Comment on the morphology of the erythrocytes.
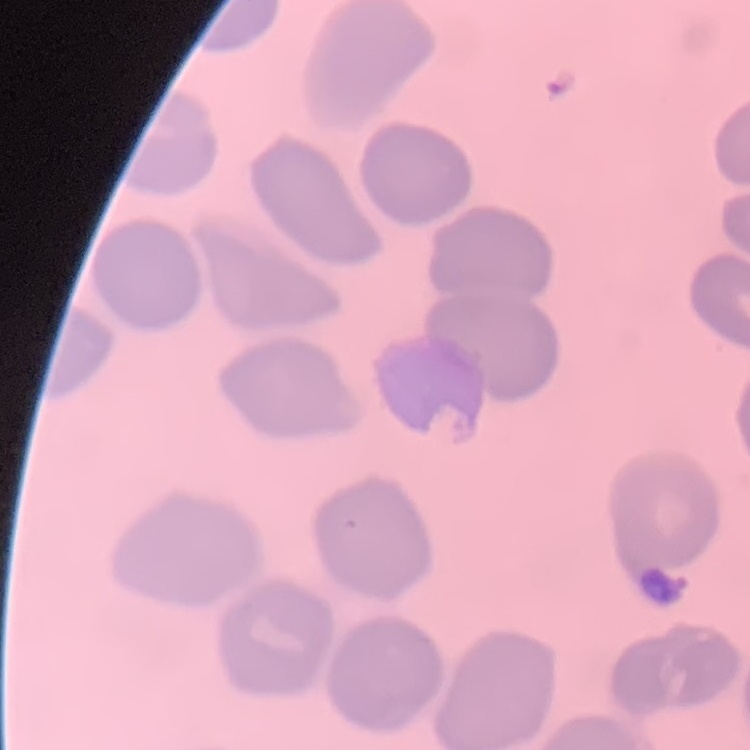

They show no rouleaux formation.

Summary:
  - Image type: one tile cut from a larger photomicrograph
  - Stain: Field's or Giemsa
  - Preparation: thin blood film